Assess this cell for malaria.
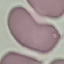

It is uninfected.

Summary:
  - Preparation: thin blood film
  - Capture: smartphone camera at the microscope eyepiece
  - Image type: automatically extracted cell patch, resized to 64 × 64 pixels
  - Stain: Giemsa